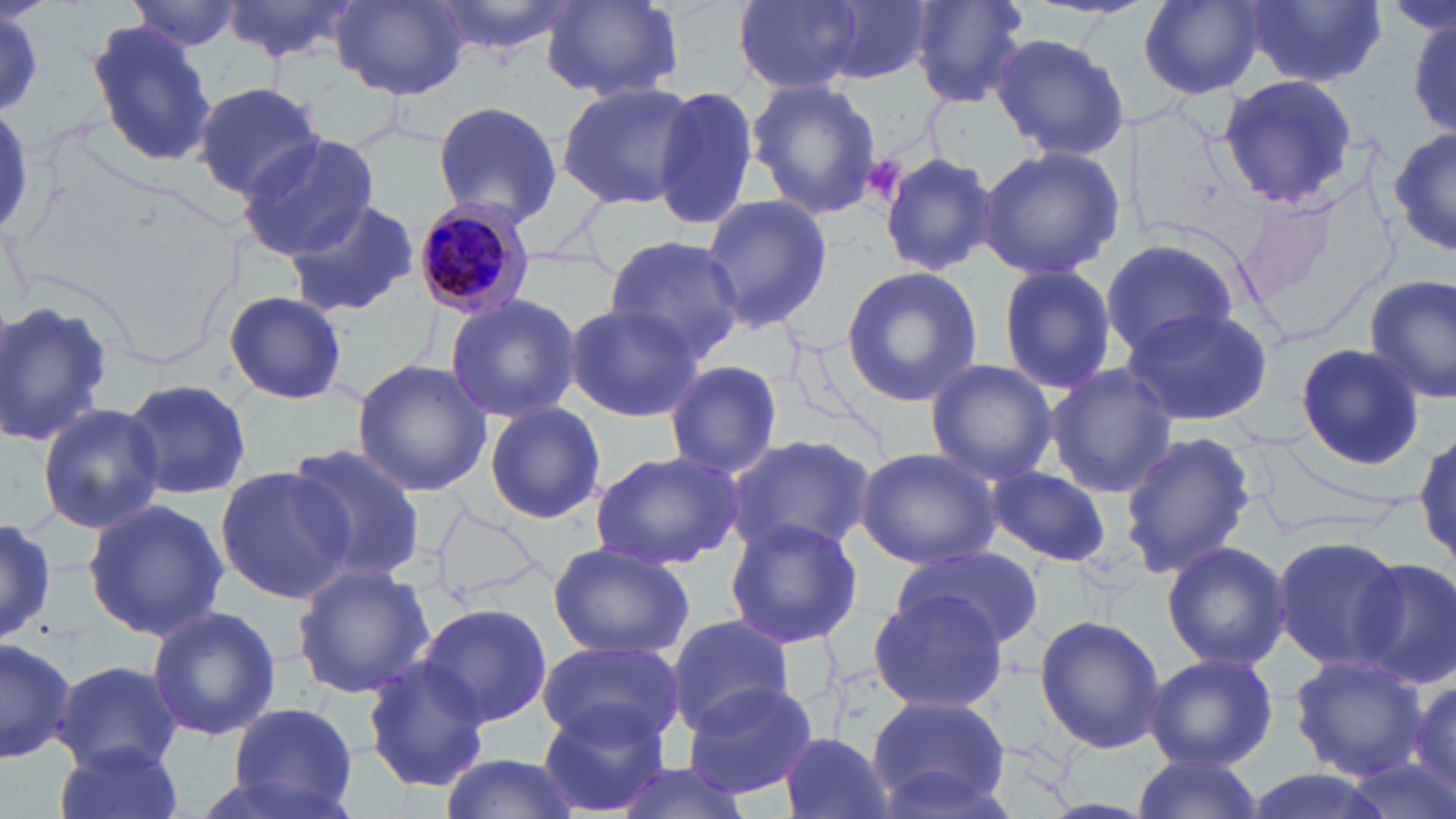

slide-level diagnosis = Plasmodium malariae
image size = 1456×819 pixels
uninfected red blood cell locations = approximate bounding boxes as named x1/y1/x2/y2 corners in pixels: (x1=218, y1=0, x2=365, y2=67), (x1=344, y1=0, x2=553, y2=74), (x1=427, y1=0, x2=578, y2=60), (x1=539, y1=0, x2=685, y2=103), (x1=730, y1=0, x2=869, y2=94), (x1=817, y1=0, x2=940, y2=84), (x1=909, y1=0, x2=1034, y2=107), (x1=1137, y1=0, x2=1267, y2=99), (x1=1241, y1=0, x2=1389, y2=86), (x1=128, y1=1, x2=244, y2=51), (x1=332, y1=1, x2=471, y2=101), (x1=0, y1=9, x2=45, y2=112), (x1=1407, y1=12, x2=1455, y2=138), (x1=85, y1=19, x2=217, y2=170), (x1=987, y1=32, x2=1131, y2=161), (x1=1216, y1=74, x2=1357, y2=210), (x1=747, y1=79, x2=883, y2=219), (x1=193, y1=80, x2=326, y2=203), (x1=556, y1=82, x2=699, y2=210), (x1=652, y1=83, x2=759, y2=232), (x1=431, y1=99, x2=565, y2=224), (x1=1390, y1=127, x2=1456, y2=258), (x1=236, y1=133, x2=380, y2=259), (x1=975, y1=144, x2=1126, y2=282), (x1=879, y1=151, x2=996, y2=278), (x1=698, y1=193, x2=834, y2=336), (x1=284, y1=198, x2=418, y2=318), (x1=1099, y1=236, x2=1241, y2=359), (x1=603, y1=237, x2=745, y2=363), (x1=996, y1=263, x2=1117, y2=398), (x1=839, y1=266, x2=984, y2=408), (x1=1361, y1=274, x2=1456, y2=407), (x1=221, y1=289, x2=349, y2=404), (x1=442, y1=293, x2=582, y2=423), (x1=0, y1=299, x2=112, y2=447), (x1=563, y1=302, x2=705, y2=424), (x1=1118, y1=305, x2=1274, y2=428), (x1=1293, y1=341, x2=1426, y2=468), (x1=351, y1=358, x2=491, y2=497), (x1=662, y1=359, x2=785, y2=479), (x1=923, y1=360, x2=1061, y2=483), (x1=1045, y1=363, x2=1178, y2=500), (x1=117, y1=378, x2=253, y2=501), (x1=483, y1=400, x2=606, y2=525), (x1=36, y1=403, x2=164, y2=535), (x1=1413, y1=428, x2=1456, y2=571), (x1=1119, y1=430, x2=1256, y2=579), (x1=727, y1=433, x2=877, y2=556), (x1=282, y1=442, x2=426, y2=581), (x1=854, y1=446, x2=1003, y2=569), (x1=587, y1=448, x2=743, y2=572), (x1=214, y1=464, x2=353, y2=605), (x1=988, y1=466, x2=1111, y2=566), (x1=81, y1=497, x2=228, y2=642), (x1=0, y1=515, x2=55, y2=643), (x1=723, y1=517, x2=865, y2=649), (x1=1270, y1=533, x2=1408, y2=673), (x1=1160, y1=540, x2=1291, y2=672), (x1=890, y1=541, x2=1045, y2=649), (x1=547, y1=542, x2=695, y2=659), (x1=1355, y1=558, x2=1456, y2=692), (x1=293, y1=565, x2=435, y2=698), (x1=867, y1=589, x2=1012, y2=713), (x1=416, y1=602, x2=553, y2=727), (x1=144, y1=605, x2=283, y2=744), (x1=1034, y1=614, x2=1167, y2=756), (x1=665, y1=616, x2=799, y2=733), (x1=0, y1=634, x2=77, y2=761), (x1=535, y1=641, x2=685, y2=747), (x1=1143, y1=652, x2=1278, y2=770), (x1=1288, y1=654, x2=1429, y2=780), (x1=360, y1=657, x2=491, y2=792), (x1=52, y1=659, x2=183, y2=774), (x1=682, y1=678, x2=821, y2=802), (x1=1406, y1=679, x2=1456, y2=799), (x1=865, y1=692, x2=1015, y2=812), (x1=538, y1=701, x2=669, y2=815), (x1=226, y1=702, x2=361, y2=817), (x1=777, y1=732, x2=895, y2=819), (x1=53, y1=742, x2=184, y2=819), (x1=437, y1=751, x2=586, y2=819), (x1=1129, y1=752, x2=1260, y2=819), (x1=608, y1=760, x2=754, y2=819), (x1=1240, y1=767, x2=1398, y2=819), (x1=178, y1=769, x2=352, y2=819)
magnification = 1000x
stain = May-Grünwald-Giemsa
modality = optical microscopy
Plasmodium malariae-infected red blood cell locations = approximate bounding boxes as named x1/y1/x2/y2 corners in pixels: (x1=415, y1=195, x2=546, y2=313)
preparation = thin blood smear
platelet locations = approximate bounding boxes as named x1/y1/x2/y2 corners in pixels: (x1=866, y1=153, x2=908, y2=198)
field of view = one of a larger specimen